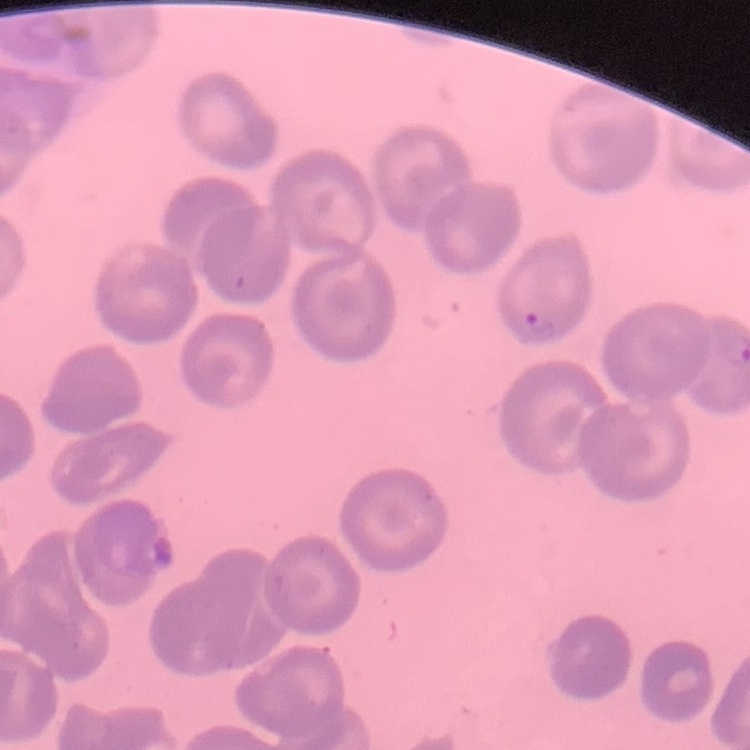
The red blood cells exhibit no rouleaux formation. Field's or Giemsa stain. Square crop of a larger photomicrograph. Thin peripheral smear.